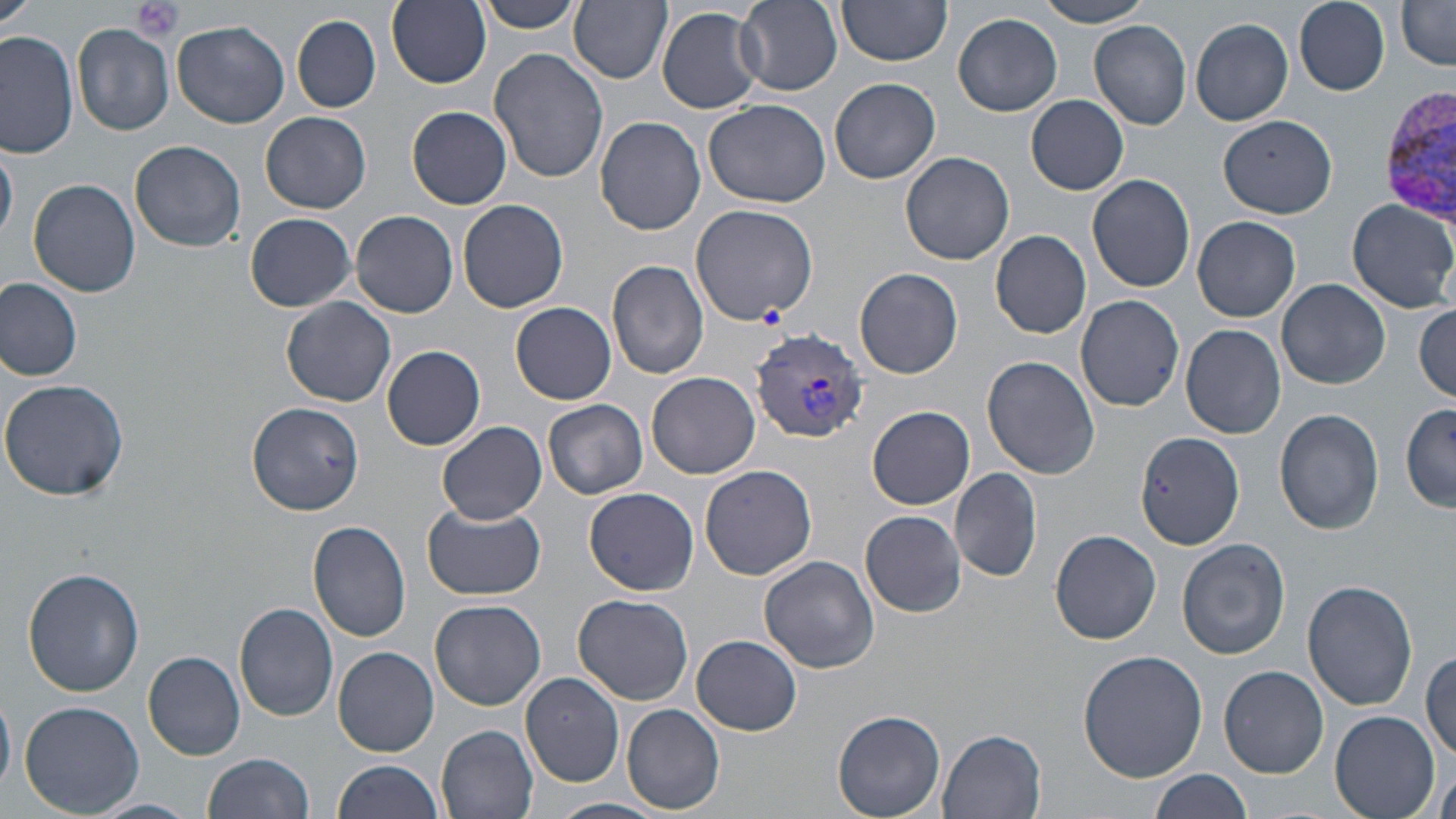

{
  "slide_level_diagnosis": "Plasmodium vivax",
  "field_of_view": "one of a larger specimen",
  "preparation": "thin blood film",
  "image_size": "1456×819 pixels",
  "platelet_locations": "approximate bounding boxes as (x1, y1, x2, y2) in pixels: (133, 0, 185, 42)",
  "modality": "optical microscopy",
  "plasmodium_vivax_infected_red_blood_cell_locations": "approximate bounding boxes as (x1, y1, x2, y2) in pixels: (1378, 84, 1456, 225), (750, 326, 871, 442)",
  "magnification": "1000x",
  "stain": "May-Grünwald-Giemsa",
  "uninfected_red_blood_cell_locations": "approximate bounding boxes as (x1, y1, x2, y2) in pixels: (1, 0, 35, 37), (478, 0, 583, 33), (569, 0, 672, 83), (737, 0, 842, 93), (838, 0, 953, 67), (1035, 0, 1158, 27), (1295, 0, 1390, 93), (386, 1, 491, 88), (1395, 2, 1456, 70), (657, 6, 765, 114), (952, 12, 1063, 117), (292, 14, 381, 113), (1190, 18, 1294, 125), (172, 20, 290, 130), (1089, 20, 1191, 130), (73, 24, 174, 136), (0, 30, 78, 159), (488, 48, 608, 185), (829, 77, 942, 184), (1026, 94, 1130, 195), (703, 99, 832, 207), (407, 106, 512, 209), (261, 111, 371, 214), (1218, 115, 1339, 219), (595, 116, 705, 236), (130, 139, 247, 252), (1, 141, 19, 247), (901, 150, 1014, 265), (1087, 174, 1195, 293), (28, 179, 140, 296), (1346, 198, 1456, 313), (458, 200, 568, 314), (689, 205, 819, 326), (352, 211, 458, 317), (245, 212, 356, 312), (1192, 216, 1301, 322), (990, 230, 1092, 339), (608, 260, 710, 379), (855, 267, 963, 380), (0, 276, 84, 380), (1277, 279, 1391, 389), (1075, 293, 1184, 411), (282, 298, 397, 407), (511, 302, 616, 404), (1413, 302, 1456, 401), (1180, 324, 1286, 438), (381, 345, 485, 451), (983, 355, 1101, 478), (647, 371, 760, 478), (0, 379, 129, 501), (542, 398, 648, 499), (247, 401, 364, 515), (1400, 403, 1454, 512), (867, 405, 975, 508), (1274, 408, 1387, 535), (437, 422, 547, 524), (1135, 432, 1244, 550), (699, 464, 817, 580), (950, 468, 1043, 583), (584, 487, 699, 596), (419, 499, 547, 598), (860, 511, 966, 618), (308, 519, 411, 642), (1049, 529, 1162, 644), (1177, 538, 1290, 660), (760, 554, 880, 674), (21, 567, 144, 697), (1302, 579, 1418, 711), (573, 593, 693, 705), (429, 599, 546, 711), (235, 602, 338, 722), (692, 635, 802, 735), (334, 647, 440, 756), (1422, 647, 1455, 762), (1077, 649, 1207, 782), (143, 650, 246, 761), (1220, 665, 1329, 778), (520, 671, 626, 787), (19, 702, 145, 817), (622, 704, 725, 815), (831, 709, 947, 818), (1330, 711, 1440, 819), (436, 725, 540, 819), (935, 728, 1049, 818), (202, 753, 315, 819), (333, 759, 443, 818), (1435, 768, 1456, 819), (1149, 769, 1256, 819), (551, 797, 669, 819), (91, 798, 199, 819)"
}